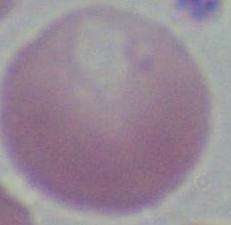 Micrograph. 1000x magnification. A red blood cell is seen.